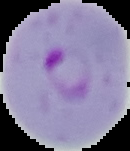
From a thin blood film. Image is 130×151 pixels. Malaria status: parasitized. Cell region segmented out of the field of view; the surrounding area is masked to black.